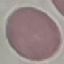
malaria status = uninfected
stain = Giemsa
preparation = thin blood smear
capture = smartphone through the microscope eyepiece
image type = cell patch, automatically extracted from a larger field of view and resized to 64 × 64 pixels